Assess this cell for malaria.
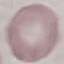
It is uninfected.

preparation = thin blood smear
capture = smartphone through the microscope eyepiece
stain = Giemsa
image type = cell patch, automatically extracted from a larger field of view and resized to 64 × 64 pixels